Identify the parasite.
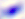

This is Toxoplasma gondii.

modality = micrograph
magnification = 400x